Outline each Plasmodium vivax-infected red blood cell.
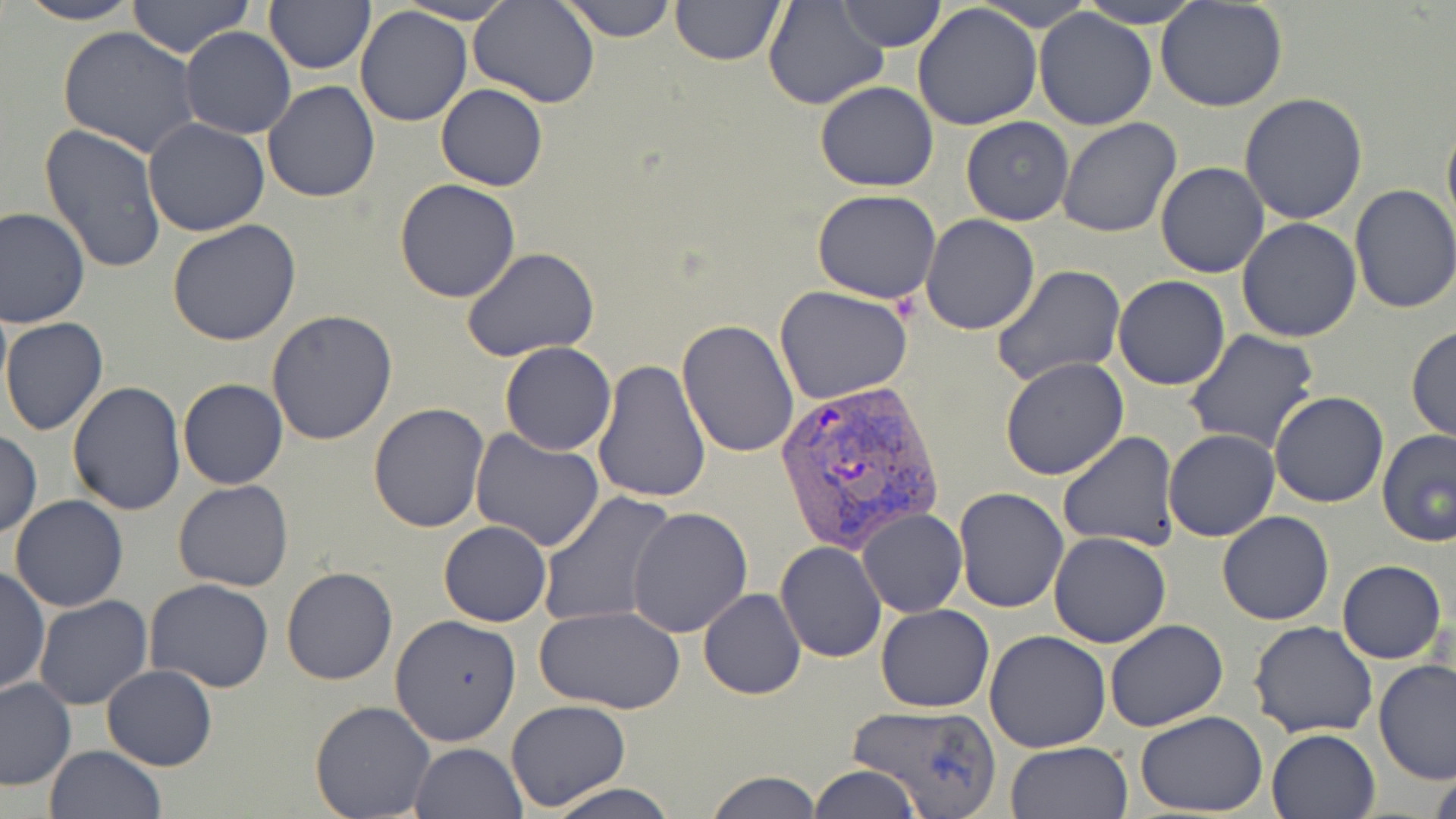
Approximate bounding boxes as named x1/y1/x2/y2 corners in pixels.
Plasmodium vivax-infected red blood cells: (x1=775, y1=378, x2=946, y2=559).

{
  "slide_level_diagnosis": "Plasmodium vivax",
  "magnification": "1000x",
  "preparation": "thin blood smear",
  "modality": "light microscopy",
  "image_size": "1456×819 pixels",
  "uninfected_red_blood_cell_locations": "approximate bounding boxes as named x1/y1/x2/y2 corners in pixels: (x1=15, y1=0, x2=143, y2=25), (x1=126, y1=0, x2=255, y2=60), (x1=265, y1=0, x2=375, y2=75), (x1=469, y1=0, x2=600, y2=107), (x1=561, y1=0, x2=676, y2=42), (x1=670, y1=0, x2=784, y2=65), (x1=837, y1=0, x2=944, y2=50), (x1=978, y1=0, x2=1093, y2=31), (x1=1077, y1=1, x2=1204, y2=27), (x1=1157, y1=1, x2=1289, y2=112), (x1=396, y1=2, x2=518, y2=24), (x1=762, y1=2, x2=888, y2=111), (x1=913, y1=4, x2=1043, y2=132), (x1=354, y1=7, x2=473, y2=127), (x1=1033, y1=8, x2=1158, y2=130), (x1=56, y1=27, x2=201, y2=158), (x1=181, y1=27, x2=295, y2=139), (x1=263, y1=81, x2=380, y2=203), (x1=814, y1=81, x2=938, y2=192), (x1=436, y1=84, x2=548, y2=192), (x1=1240, y1=94, x2=1368, y2=225), (x1=1441, y1=109, x2=1456, y2=242), (x1=961, y1=116, x2=1074, y2=226), (x1=1059, y1=118, x2=1184, y2=238), (x1=142, y1=119, x2=270, y2=237), (x1=38, y1=125, x2=166, y2=275), (x1=1155, y1=162, x2=1269, y2=277), (x1=394, y1=178, x2=523, y2=302), (x1=1349, y1=184, x2=1456, y2=314), (x1=811, y1=189, x2=942, y2=304), (x1=0, y1=208, x2=90, y2=330), (x1=920, y1=215, x2=1039, y2=334), (x1=1237, y1=217, x2=1363, y2=341), (x1=167, y1=220, x2=302, y2=346), (x1=462, y1=248, x2=600, y2=361), (x1=995, y1=265, x2=1127, y2=385), (x1=1113, y1=275, x2=1231, y2=390), (x1=775, y1=285, x2=914, y2=404), (x1=266, y1=309, x2=400, y2=446), (x1=2, y1=317, x2=108, y2=436), (x1=678, y1=318, x2=800, y2=458), (x1=1406, y1=325, x2=1456, y2=441), (x1=1185, y1=330, x2=1321, y2=453), (x1=499, y1=341, x2=616, y2=455), (x1=1000, y1=357, x2=1130, y2=479), (x1=592, y1=360, x2=711, y2=504), (x1=178, y1=378, x2=288, y2=489), (x1=68, y1=381, x2=186, y2=515), (x1=1269, y1=391, x2=1391, y2=509), (x1=368, y1=404, x2=491, y2=533), (x1=1164, y1=429, x2=1279, y2=541), (x1=1376, y1=429, x2=1456, y2=547), (x1=0, y1=430, x2=43, y2=538), (x1=469, y1=430, x2=605, y2=552), (x1=1060, y1=431, x2=1181, y2=552), (x1=173, y1=480, x2=294, y2=592), (x1=954, y1=487, x2=1068, y2=612), (x1=537, y1=491, x2=678, y2=631), (x1=9, y1=494, x2=129, y2=612), (x1=626, y1=508, x2=753, y2=638), (x1=859, y1=508, x2=967, y2=617), (x1=1217, y1=512, x2=1334, y2=625), (x1=439, y1=520, x2=551, y2=627), (x1=1048, y1=532, x2=1170, y2=647), (x1=775, y1=541, x2=886, y2=662), (x1=1337, y1=559, x2=1445, y2=663), (x1=1, y1=565, x2=50, y2=697), (x1=280, y1=565, x2=398, y2=685), (x1=143, y1=578, x2=276, y2=693), (x1=698, y1=588, x2=806, y2=700), (x1=33, y1=596, x2=155, y2=711), (x1=876, y1=603, x2=994, y2=713), (x1=534, y1=606, x2=687, y2=713), (x1=391, y1=613, x2=522, y2=746), (x1=1104, y1=620, x2=1229, y2=733), (x1=1249, y1=621, x2=1378, y2=738), (x1=984, y1=631, x2=1112, y2=752), (x1=1374, y1=661, x2=1456, y2=786), (x1=101, y1=665, x2=218, y2=771), (x1=0, y1=677, x2=75, y2=791), (x1=504, y1=699, x2=631, y2=812), (x1=310, y1=701, x2=436, y2=819), (x1=846, y1=703, x2=1005, y2=819), (x1=1135, y1=711, x2=1269, y2=816), (x1=1266, y1=727, x2=1381, y2=819), (x1=1005, y1=741, x2=1131, y2=819), (x1=410, y1=742, x2=526, y2=819), (x1=44, y1=746, x2=167, y2=819), (x1=1427, y1=763, x2=1456, y2=819), (x1=808, y1=765, x2=920, y2=819), (x1=705, y1=771, x2=821, y2=818), (x1=543, y1=781, x2=678, y2=819)",
  "stain": "May-Grünwald-Giemsa",
  "field_of_view": "single"
}